Classify this cell by malaria status.
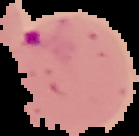

Parasitized.

Segmented cell region on a black background. From a thin blood film. Image is 139×136 pixels.